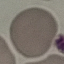
malaria status = uninfected
capture = smartphone camera at the microscope eyepiece
preparation = thin blood film
image type = cell patch, automatically extracted from a larger field of view and resized to 64 × 64 pixels
stain = Giemsa